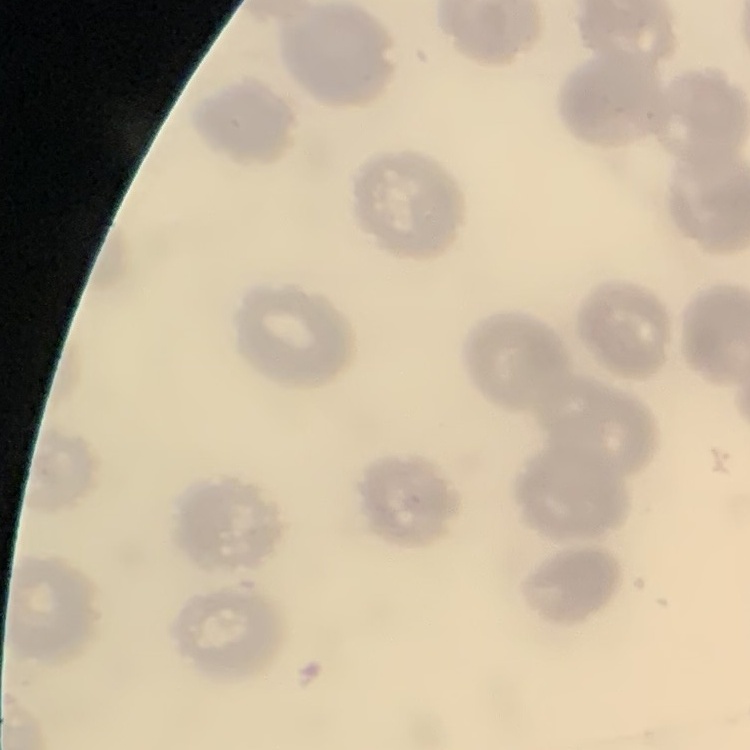
erythrocyte morphology = no rouleaux formation
preparation = thin peripheral smear
stain = Field's or Giemsa
image type = one tile cut from a larger photomicrograph